Locate platelets.
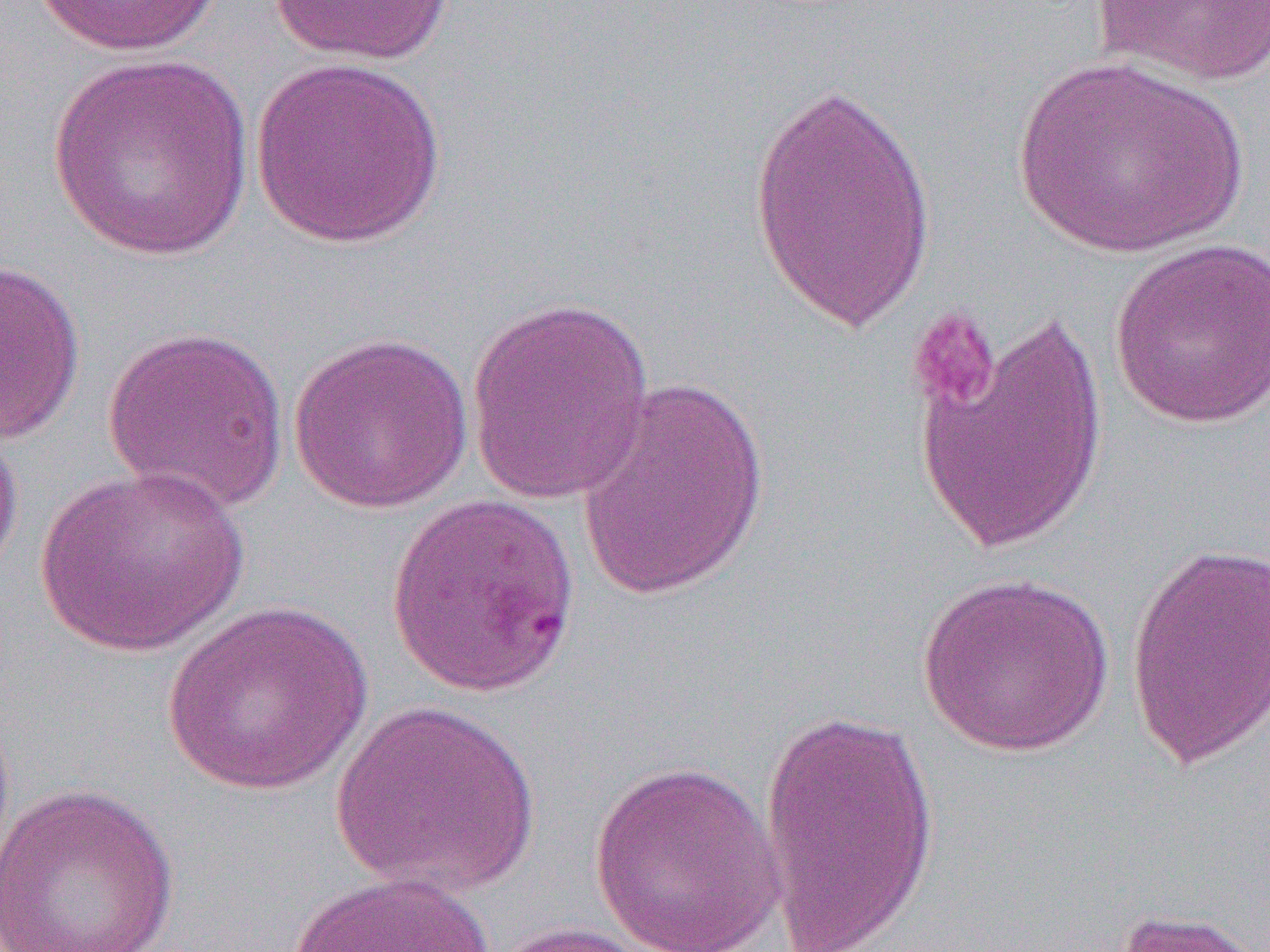
Approximate bounding boxes as (x1, y1, x2, y2) in pixels.
Platelets: (907, 306, 1002, 416).

slide-level diagnosis = Plasmodium falciparum
field of view = one of a larger specimen
magnification = 1000x
image size = 1270×952 pixels
modality = optical microscopy
uninfected red blood cell locations = approximate bounding boxes as (x1, y1, x2, y2) in pixels: (32, 0, 223, 57), (266, 0, 457, 66), (1093, 0, 1270, 87), (46, 53, 256, 261), (1011, 55, 1252, 258), (249, 56, 448, 249), (746, 75, 941, 335), (1107, 238, 1270, 430), (0, 257, 86, 445), (465, 296, 658, 504), (910, 308, 1113, 557), (101, 325, 291, 515), (287, 331, 475, 514), (573, 377, 773, 603), (0, 411, 23, 589), (33, 465, 250, 658), (385, 492, 583, 698), (1124, 540, 1270, 772), (917, 571, 1114, 756), (159, 599, 375, 796), (329, 698, 543, 897), (757, 708, 942, 952), (588, 760, 789, 952), (0, 781, 181, 952), (288, 870, 497, 952), (1108, 907, 1265, 952), (482, 921, 676, 952)
preparation = thin blood film